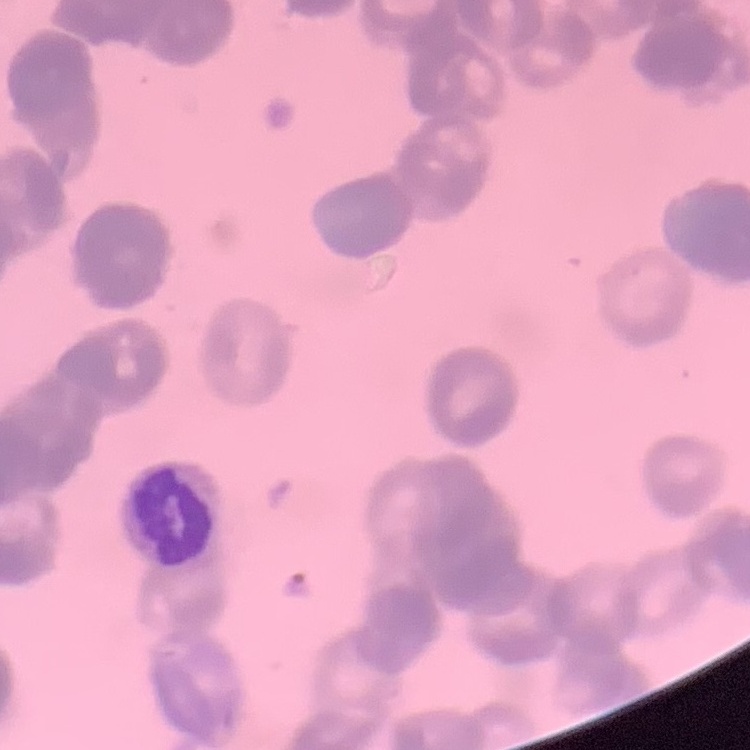

The red blood cells exhibit rouleaux formation. Thin peripheral smear. Stained with either Field's or Giemsa. Square crop of a larger photomicrograph.